Classify this cell by malaria status.
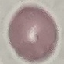

Uninfected.

Giemsa stain. Photographed with a smartphone camera at the microscope eyepiece. Thin blood film. Cell patch, automatically extracted from a larger field of view and resized to 64 × 64 pixels.